Outline each blood parasite and name the species.
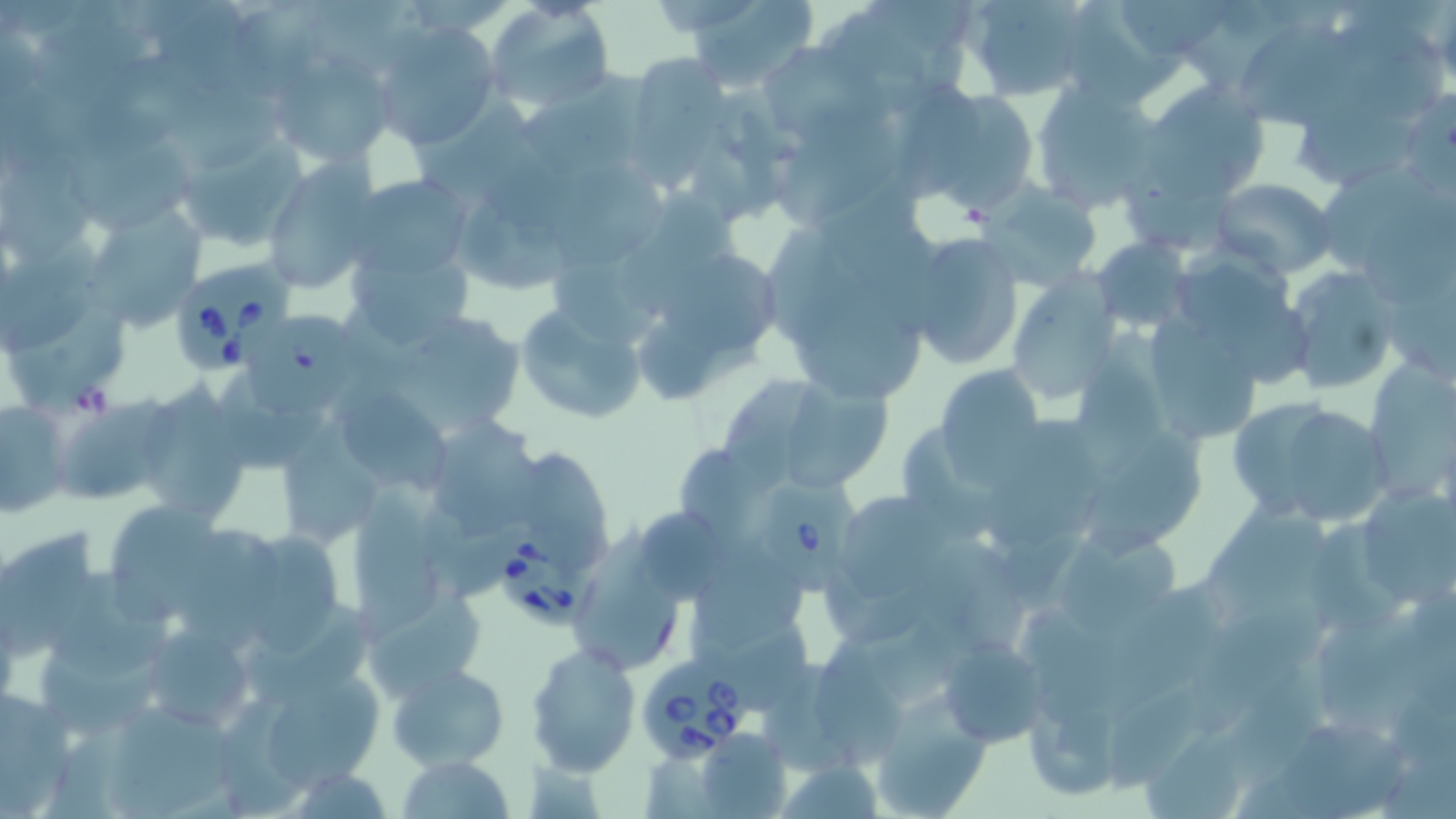
Approximate bounding boxes as named x1/y1/x2/y2 corners in pixels.
Babesia divergens-infected red blood cells: (x1=172, y1=256, x2=299, y2=368), (x1=755, y1=471, x2=864, y2=596), (x1=493, y1=531, x2=605, y2=624), (x1=637, y1=654, x2=753, y2=762).
No Plasmodium falciparum, Plasmodium ovale, Plasmodium malariae, Plasmodium vivax, or Trypanosoma brucei observed.

{
  "slide_level_diagnosis": "Babesia divergens",
  "modality": "light microscopy",
  "magnification": "1000x",
  "image_size": "1456×819 pixels",
  "preparation": "thin blood film",
  "field_of_view": "one of a larger specimen",
  "uninfected_red_blood_cell_locations": "approximate bounding boxes as named x1/y1/x2/y2 corners in pixels: (x1=163, y1=0, x2=240, y2=97), (x1=681, y1=0, x2=820, y2=91), (x1=961, y1=0, x2=1096, y2=100), (x1=1119, y1=0, x2=1236, y2=63), (x1=484, y1=2, x2=614, y2=112), (x1=1074, y1=5, x2=1186, y2=104), (x1=844, y1=11, x2=929, y2=117), (x1=238, y1=13, x2=316, y2=101), (x1=373, y1=18, x2=502, y2=149), (x1=33, y1=22, x2=153, y2=108), (x1=1339, y1=22, x2=1452, y2=123), (x1=1234, y1=24, x2=1371, y2=126), (x1=760, y1=41, x2=859, y2=141), (x1=267, y1=51, x2=398, y2=167), (x1=81, y1=54, x2=206, y2=165), (x1=639, y1=56, x2=726, y2=199), (x1=521, y1=72, x2=657, y2=180), (x1=1138, y1=81, x2=1273, y2=201), (x1=1031, y1=84, x2=1164, y2=211), (x1=905, y1=85, x2=1042, y2=211), (x1=1297, y1=93, x2=1418, y2=186), (x1=417, y1=96, x2=542, y2=210), (x1=787, y1=114, x2=901, y2=224), (x1=177, y1=133, x2=309, y2=256), (x1=73, y1=145, x2=192, y2=224), (x1=261, y1=157, x2=382, y2=293), (x1=1321, y1=159, x2=1448, y2=260), (x1=1, y1=161, x2=94, y2=265), (x1=559, y1=165, x2=667, y2=267), (x1=344, y1=174, x2=475, y2=281), (x1=1210, y1=178, x2=1336, y2=274), (x1=985, y1=184, x2=1104, y2=293), (x1=623, y1=194, x2=743, y2=313), (x1=462, y1=200, x2=585, y2=287), (x1=88, y1=202, x2=207, y2=333), (x1=1365, y1=202, x2=1456, y2=306), (x1=766, y1=228, x2=873, y2=356), (x1=900, y1=232, x2=1027, y2=371), (x1=1092, y1=237, x2=1191, y2=330), (x1=1, y1=240, x2=102, y2=359), (x1=347, y1=245, x2=476, y2=350), (x1=659, y1=247, x2=793, y2=356), (x1=555, y1=260, x2=660, y2=350), (x1=1282, y1=266, x2=1401, y2=395), (x1=1007, y1=274, x2=1122, y2=407), (x1=513, y1=304, x2=648, y2=426), (x1=797, y1=306, x2=926, y2=407), (x1=250, y1=314, x2=364, y2=415), (x1=1148, y1=316, x2=1259, y2=440), (x1=12, y1=317, x2=127, y2=414), (x1=399, y1=317, x2=527, y2=424), (x1=639, y1=327, x2=761, y2=402), (x1=1075, y1=331, x2=1166, y2=476), (x1=1371, y1=357, x2=1456, y2=500), (x1=934, y1=364, x2=1047, y2=478), (x1=723, y1=368, x2=822, y2=500), (x1=772, y1=377, x2=892, y2=493), (x1=134, y1=384, x2=253, y2=528), (x1=331, y1=384, x2=454, y2=493), (x1=1226, y1=394, x2=1394, y2=526), (x1=1, y1=401, x2=71, y2=519), (x1=54, y1=401, x2=169, y2=504), (x1=420, y1=414, x2=544, y2=539), (x1=289, y1=431, x2=380, y2=548), (x1=1090, y1=431, x2=1208, y2=558), (x1=528, y1=452, x2=611, y2=568), (x1=1354, y1=482, x2=1456, y2=612), (x1=844, y1=490, x2=957, y2=595), (x1=357, y1=495, x2=444, y2=643), (x1=1196, y1=496, x2=1327, y2=625), (x1=110, y1=500, x2=230, y2=626), (x1=636, y1=502, x2=727, y2=603), (x1=1312, y1=511, x2=1409, y2=638), (x1=582, y1=524, x2=685, y2=676), (x1=3, y1=528, x2=97, y2=667), (x1=1061, y1=531, x2=1182, y2=640), (x1=178, y1=533, x2=289, y2=650), (x1=253, y1=534, x2=343, y2=650), (x1=930, y1=535, x2=1028, y2=655), (x1=699, y1=541, x2=809, y2=647), (x1=56, y1=567, x2=180, y2=673), (x1=827, y1=571, x2=931, y2=646), (x1=1106, y1=586, x2=1224, y2=716), (x1=1184, y1=587, x2=1339, y2=728), (x1=363, y1=592, x2=485, y2=698), (x1=690, y1=609, x2=810, y2=714), (x1=1315, y1=619, x2=1421, y2=723), (x1=139, y1=622, x2=259, y2=733), (x1=41, y1=637, x2=157, y2=737), (x1=815, y1=637, x2=903, y2=773), (x1=940, y1=637, x2=1048, y2=747), (x1=526, y1=643, x2=640, y2=775), (x1=244, y1=653, x2=387, y2=796), (x1=387, y1=663, x2=510, y2=769), (x1=1231, y1=667, x2=1337, y2=789), (x1=1, y1=687, x2=76, y2=812), (x1=870, y1=693, x2=992, y2=818), (x1=218, y1=694, x2=309, y2=814), (x1=110, y1=702, x2=229, y2=817), (x1=1029, y1=704, x2=1122, y2=801), (x1=1286, y1=721, x2=1405, y2=819), (x1=1149, y1=726, x2=1249, y2=819), (x1=694, y1=727, x2=792, y2=817), (x1=398, y1=753, x2=516, y2=818)",
  "stain": "May-Grünwald-Giemsa"
}